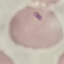
Summary:
  - Result: malaria parasites identified
  - Stain: Giemsa
  - Preparation: thin smear
  - Capture: smartphone camera at the microscope eyepiece
  - Image type: automatically extracted cell patch, resized to 64 × 64 pixels